Comment on the morphology of the red blood cells.
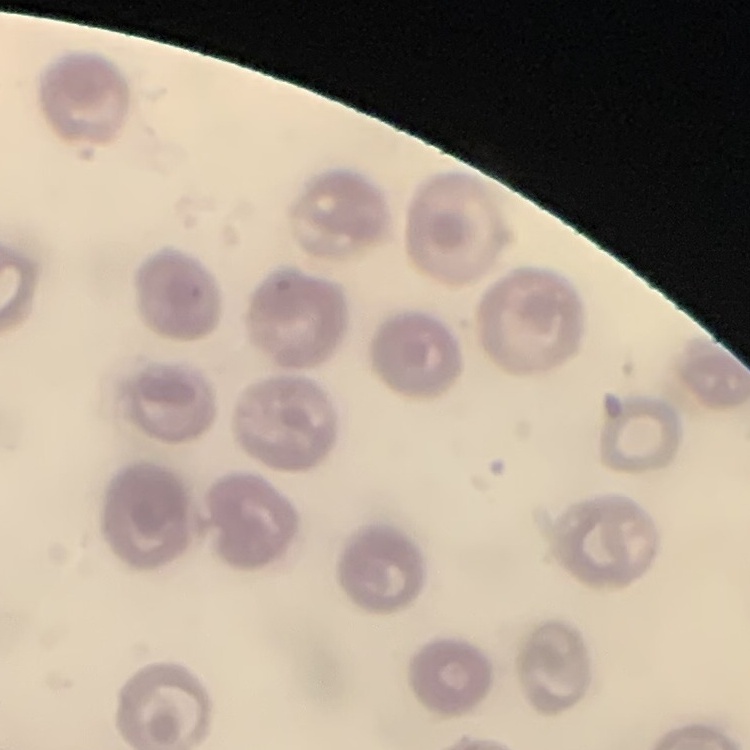

They show no rouleaux formation.

stain: Field's or Giemsa
image_type: square crop of a larger photomicrograph
preparation: thin blood film